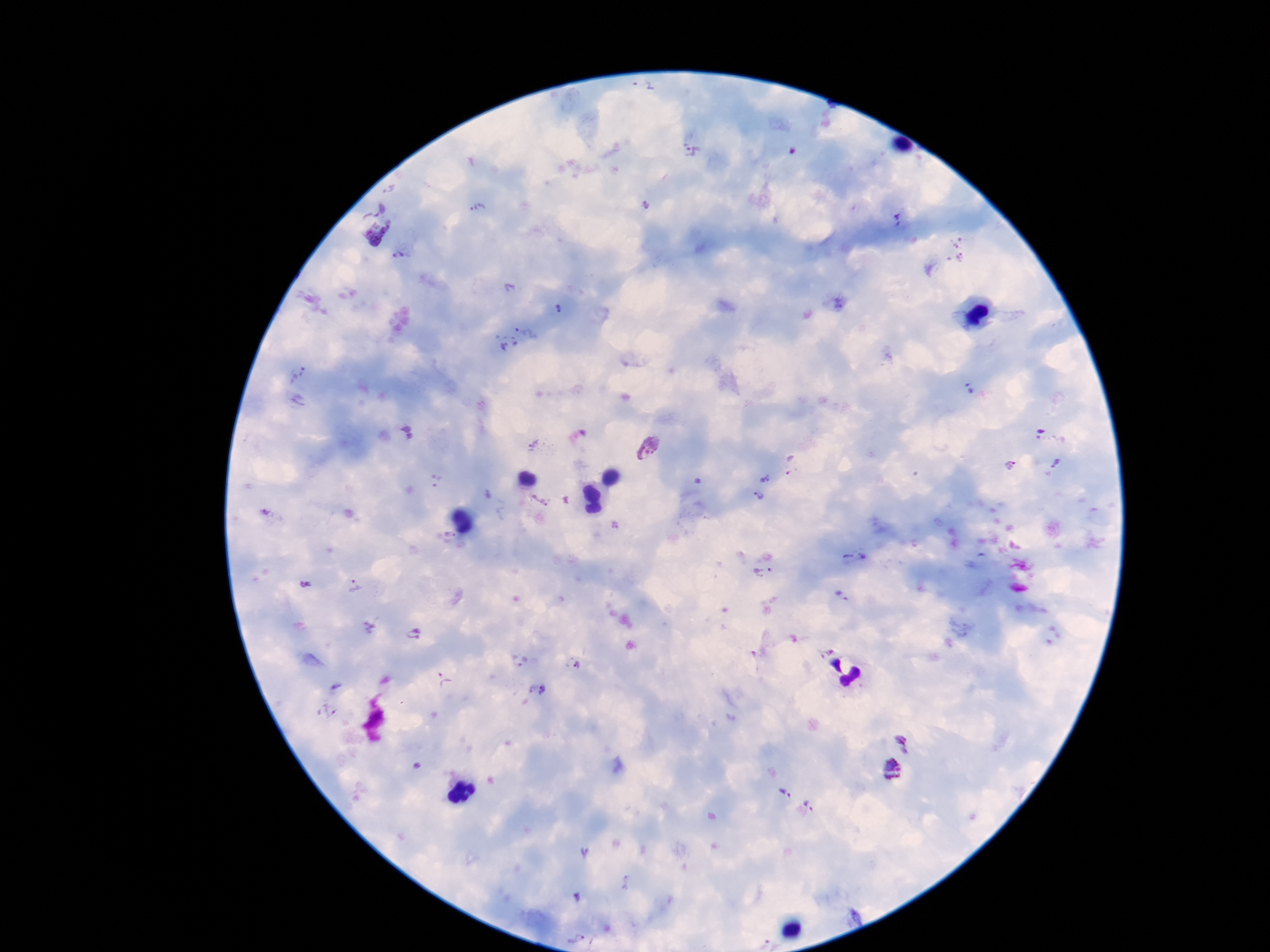
Approximate centers as {x, y} in pixels. Plasmodium parasite locations: {642, 92}, {690, 151}, {476, 210}, {898, 220}, {377, 232}, {956, 248}, {402, 258}, {515, 339}, {299, 373}, {968, 387}, {1052, 432}, {535, 445}, {646, 447}, {1057, 465}, {1010, 466}, {764, 479}, {758, 497}, {539, 500}, {450, 535}, {763, 573}, {305, 583}, {355, 586}, {842, 596}, {414, 634}, {519, 660}, {576, 666}, {445, 679}, {536, 690}, {904, 741}, {893, 770}, {783, 792}, {812, 802}, {575, 937}. Giemsa stain. Image is 1270×952 pixels. Thick blood film. One field from this slide. Patient malaria status: infected. 100x magnification. Smartphone photograph taken through the microscope eyepiece.